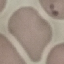

result = malaria parasites detected
capture = smartphone through the microscope eyepiece
preparation = thin blood film
stain = Giemsa
image type = cell patch, automatically extracted from a larger field of view and resized to 64 × 64 pixels